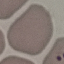 Result: no malaria parasites detected. Acquired by smartphone through the microscope eyepiece. Thin blood film. Giemsa stain. Automatically extracted cell patch, resized to 64 × 64 pixels.